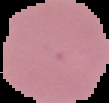

From a thin blood smear. Image is 109×103 pixels. Segmented cell region on a black background. Result: negative for Plasmodium parasites.